Report the malaria status of this cell.
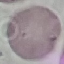
Uninfected.

preparation = thin smear
capture = smartphone camera at the microscope eyepiece
stain = Giemsa
image type = cell patch, automatically extracted from a larger field of view and resized to 64 × 64 pixels